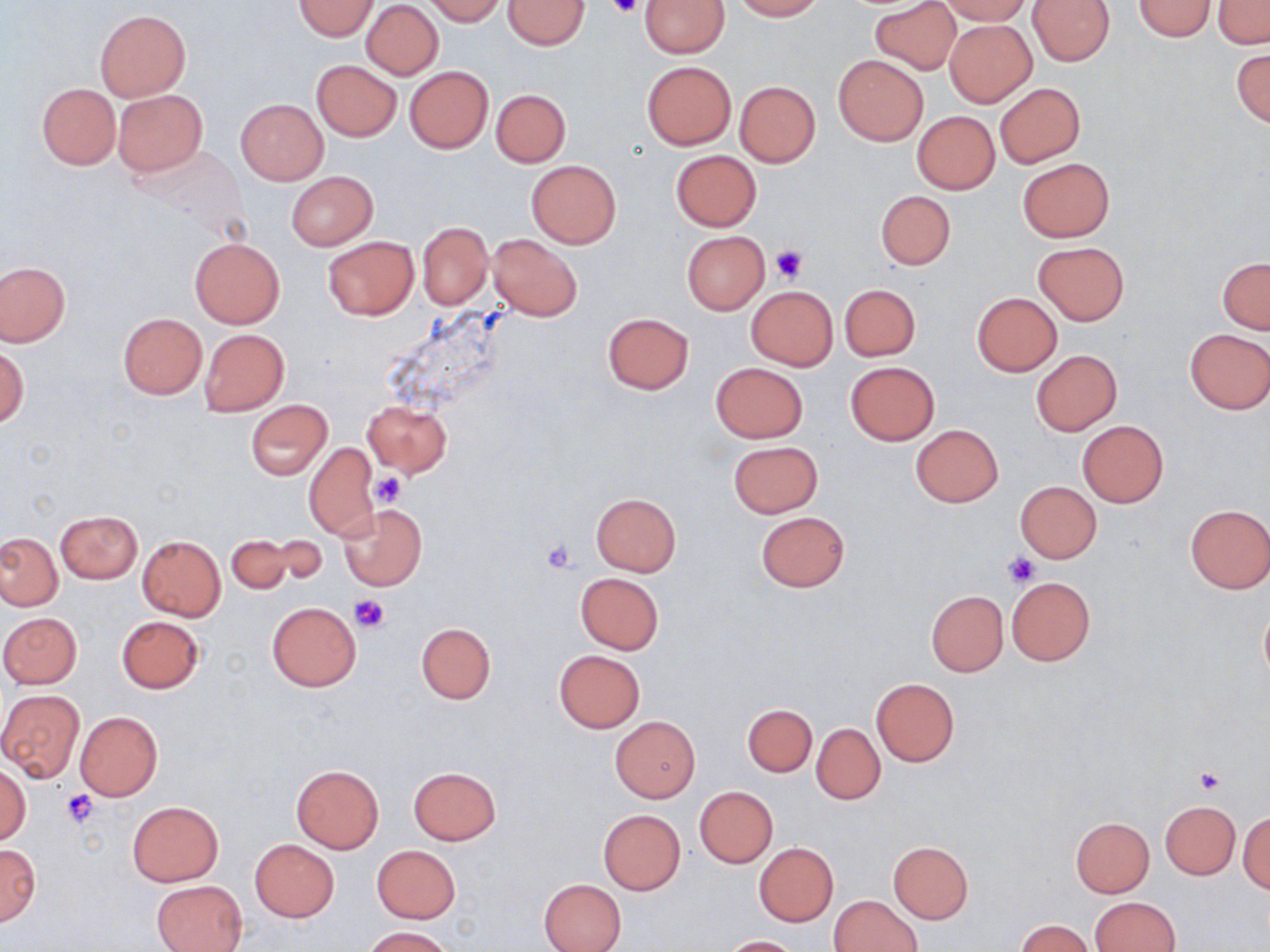 Approximate bounding boxes as [x1, y1, x2, y2] in pixels. Uninfected red blood cell locations: [423, 0, 505, 25], [503, 0, 589, 50], [641, 0, 729, 57], [732, 0, 824, 20], [870, 0, 963, 74], [938, 0, 1029, 25], [1027, 0, 1115, 66], [1133, 0, 1217, 40], [1211, 0, 1270, 48], [293, 1, 379, 40], [361, 1, 443, 79], [95, 9, 191, 102], [944, 20, 1035, 105], [1231, 49, 1270, 127], [833, 55, 929, 145], [311, 60, 401, 141], [641, 61, 736, 149], [404, 67, 493, 153], [734, 81, 820, 167], [37, 83, 120, 169], [993, 83, 1085, 167], [113, 89, 207, 176], [491, 89, 570, 166], [236, 99, 328, 184], [913, 111, 999, 194], [671, 150, 761, 230], [1018, 158, 1114, 241], [527, 161, 621, 247], [286, 171, 378, 250], [875, 190, 955, 270], [417, 222, 494, 309], [682, 232, 769, 315], [488, 234, 582, 322], [323, 236, 418, 320], [190, 239, 285, 328], [1034, 243, 1128, 325], [1218, 257, 1270, 333], [0, 262, 69, 346], [839, 283, 921, 361], [746, 287, 838, 369], [972, 293, 1062, 375], [602, 312, 694, 394], [117, 313, 207, 398], [1184, 328, 1270, 414], [200, 329, 288, 415], [1, 347, 27, 428], [1032, 350, 1122, 435], [711, 362, 808, 443], [845, 362, 939, 445], [245, 400, 332, 479], [362, 401, 452, 477], [1078, 421, 1169, 507], [910, 424, 1003, 507], [728, 440, 822, 517], [304, 441, 379, 539], [1015, 482, 1102, 563], [590, 493, 681, 577], [338, 504, 426, 591], [1184, 504, 1270, 593], [55, 510, 141, 583], [755, 511, 850, 592], [225, 532, 309, 594], [0, 533, 62, 611], [137, 535, 225, 620], [127, 539, 210, 693], [575, 573, 664, 654], [1006, 577, 1094, 665], [926, 591, 1008, 676], [267, 602, 361, 690], [1259, 603, 1270, 686], [0, 612, 82, 689], [117, 616, 203, 693], [416, 622, 495, 704], [554, 650, 644, 732], [871, 678, 959, 767], [0, 689, 85, 782], [743, 703, 816, 776], [74, 711, 163, 801], [610, 717, 700, 802], [812, 724, 884, 803], [0, 764, 31, 844], [291, 765, 384, 852], [408, 766, 501, 844], [695, 786, 777, 867], [1161, 800, 1240, 879], [127, 801, 223, 886], [597, 809, 685, 895], [1239, 814, 1269, 893], [1070, 817, 1154, 896], [250, 839, 339, 921], [888, 841, 973, 923], [0, 842, 40, 924], [753, 843, 838, 926], [371, 845, 461, 923], [540, 879, 626, 952], [151, 880, 246, 952], [831, 894, 922, 952], [1091, 897, 1180, 952], [1015, 919, 1091, 952], [361, 926, 454, 951], [721, 935, 801, 952]. Platelet locations: [607, 0, 641, 20], [771, 245, 808, 283], [372, 473, 406, 508], [541, 538, 577, 575], [1004, 551, 1037, 588], [351, 594, 390, 633], [1194, 767, 1224, 794], [62, 789, 101, 827]. Slide-level diagnosis: no evidence of blood parasites. May-Grünwald-Giemsa stain. Light microscopy. Image is 1270×952 pixels. Thin blood smear. Captured at 1000x magnification. One field of a larger specimen.